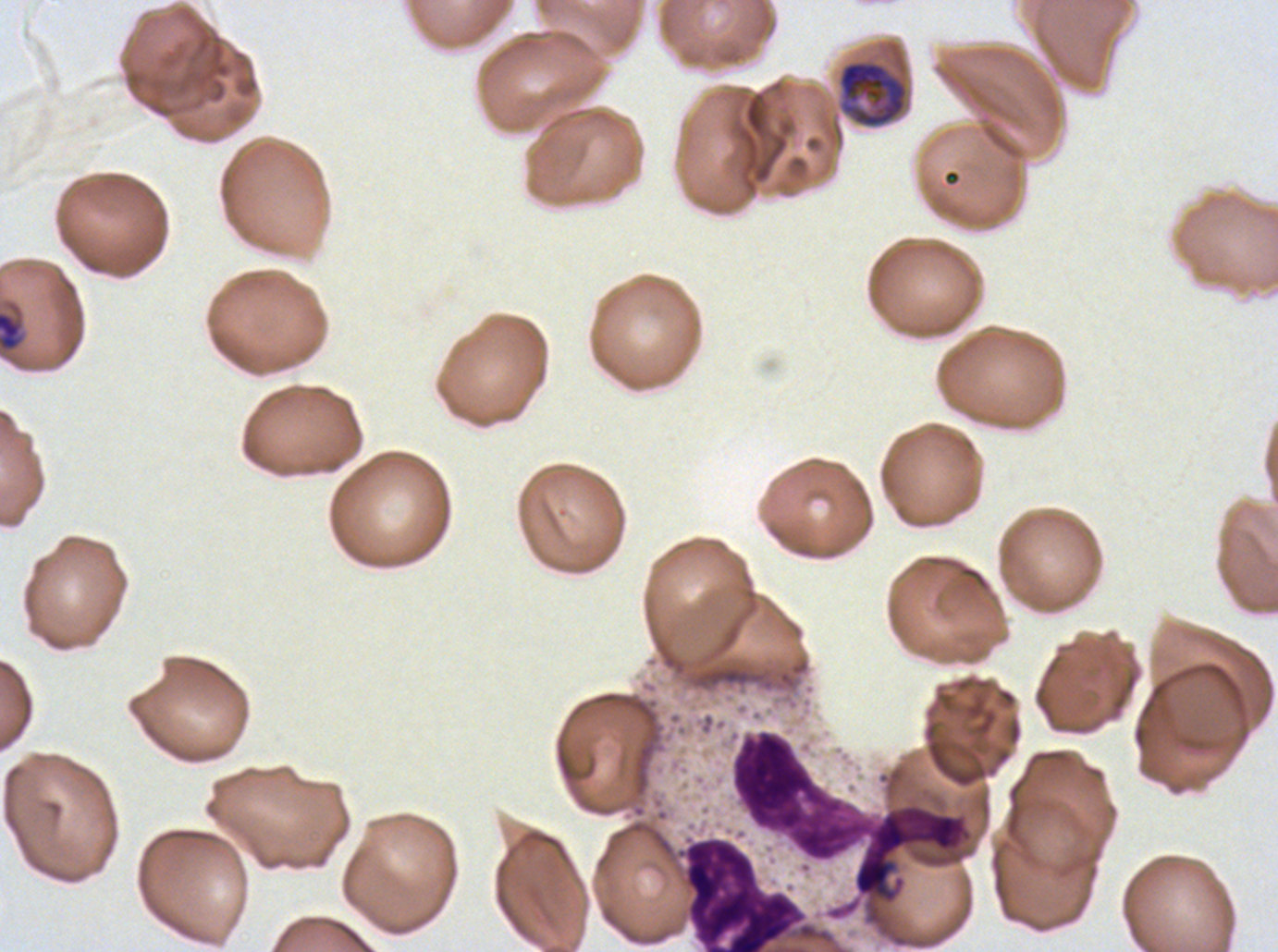
Approximate bounding boxes as {x1, y1, x2, y2} in pixels.
Summary:
  - Late trophozoite locations: {837, 60, 908, 128}
  - Late-ring/early-trophozoite locations: {0, 311, 23, 351}
  - Leukocyte locations: {731, 729, 971, 862}, {683, 836, 805, 951}
  - Field of view: one sub-image of a larger composite
  - Specimen: ex-vivo Plasmodium falciparum culture from a patient in The Gambia, grown for 24 to 48 hours
  - Image size: 1278×952 pixels
  - Preparation: thin blood film
  - Life-cycle stages observed: late-ring/early-trophozoite, late trophozoite
  - Stain: Giemsa